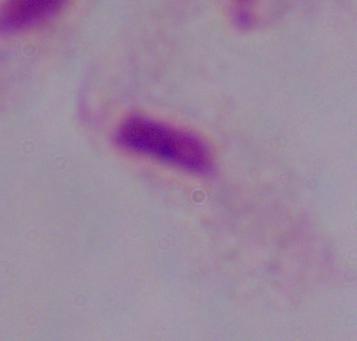
Summary:
  - Identification: trichomonad
  - Magnification: 1000x
  - Modality: micrograph